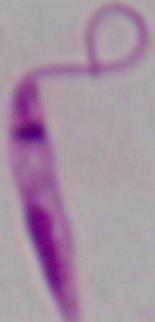
{
  "modality": "photomicrograph",
  "magnification": "1000x",
  "identification": "Leishmania"
}